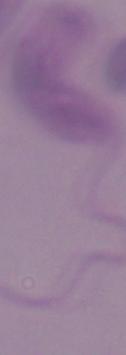
identification = Leishmania
modality = micrograph
magnification = 1000x